Name the parasite shown.
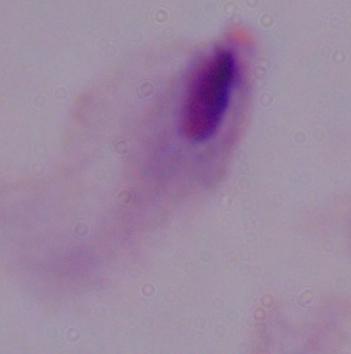
A trichomonad.

{
  "magnification": "1000x",
  "modality": "photomicrograph"
}